Locate malaria parasites and leukocytes.
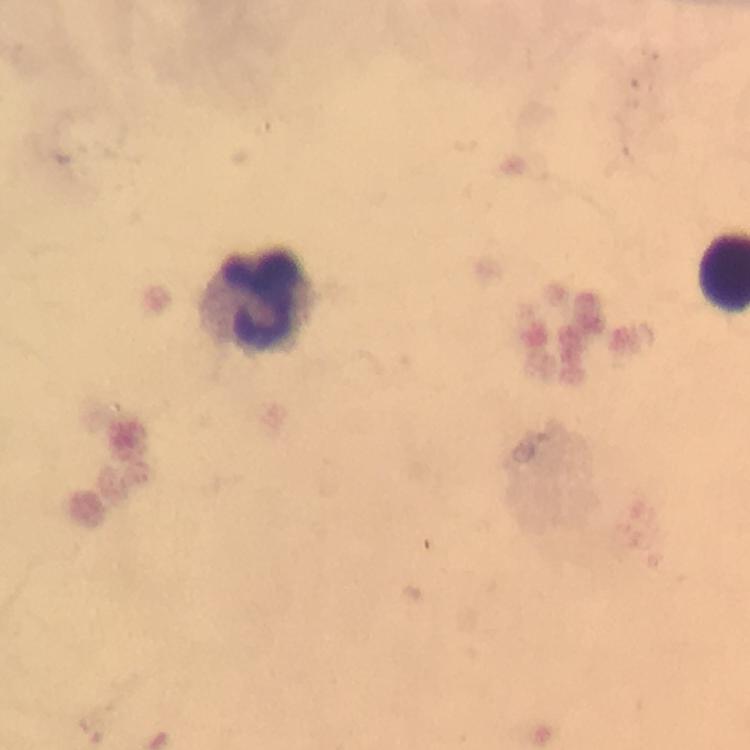

No malaria parasites seen.
Approximate centers as (x, y) in pixels.
Leukocytes: (259, 301).

Summary:
  - Stain: Giemsa
  - Cropped from: a single field of view
  - Image size: 750×750 pixels
  - Context: from a malaria diagnostic workup
  - Capture: smartphone camera through the microscope
  - Preparation: thick blood film
  - Immersion oil: used
  - Magnification: 100x